Point out each malaria parasite.
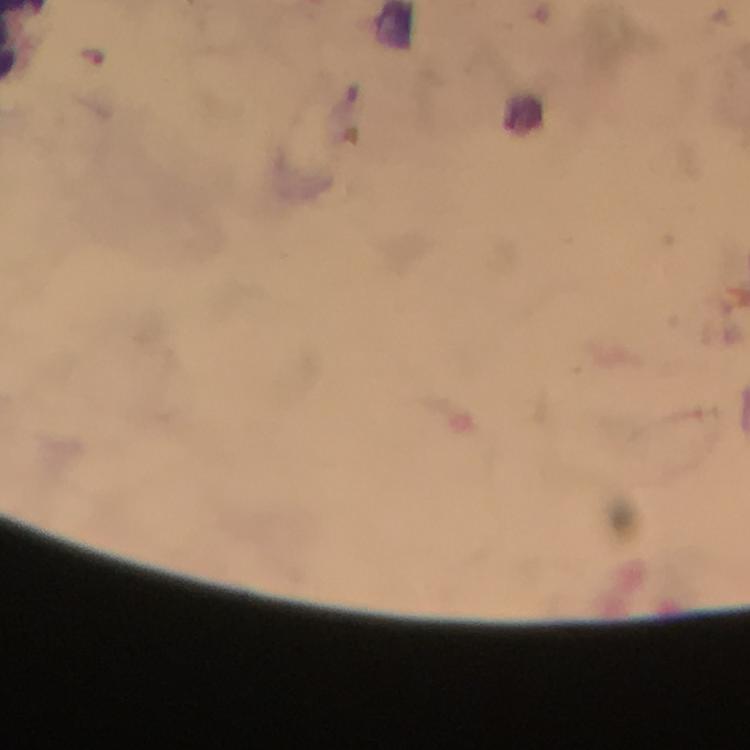

Approximate centers as (x, y) in pixels.
Malaria parasites: (96, 57).

Giemsa-stained preparation. From a malaria diagnostic workup. Photographed through the microscope with a smartphone camera. At 100x magnification. Thick blood film. Cropped region of a single field of view. Image is 750×750 pixels. Immersion oil was used.